Locate every blood parasite and identify its species.
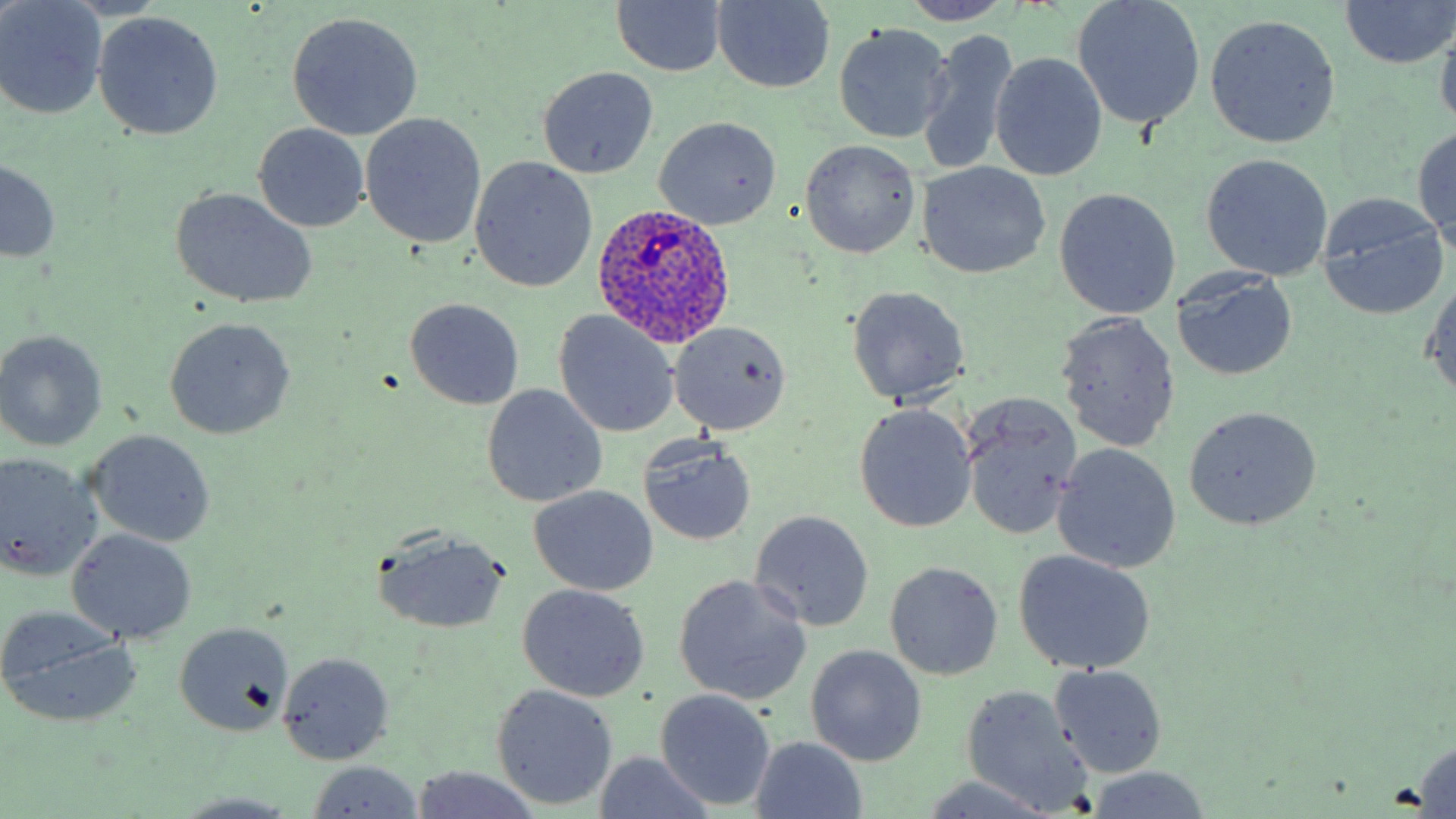

Approximate bounding boxes as (x1,y1)-(x2,y2) corner pairs in pixels.
Plasmodium ovale-infected red blood cells: (591,202)-(737,348).
No Plasmodium falciparum, Plasmodium malariae, Plasmodium vivax, Babesia divergens, or Trypanosoma brucei observed.

Uninfected red blood cell locations: (1340,0)-(1456,71), (0,1)-(107,119), (609,1)-(730,78), (900,1)-(1014,24), (1072,1)-(1206,128), (710,2)-(837,92), (286,11)-(424,140), (92,12)-(225,140), (1205,15)-(1341,147), (1434,20)-(1456,137), (834,22)-(955,144), (919,26)-(1019,177), (990,52)-(1108,182), (538,67)-(660,179), (360,112)-(487,249), (654,117)-(781,230), (1413,122)-(1455,250), (253,123)-(370,232), (800,139)-(921,259), (1200,153)-(1334,281), (469,156)-(598,292), (1,159)-(63,265), (917,161)-(1052,279), (170,188)-(318,309), (1054,188)-(1181,319), (1315,194)-(1449,319), (1172,269)-(1298,383), (1422,275)-(1456,403), (846,286)-(969,405), (405,298)-(524,410), (555,311)-(680,435), (1055,311)-(1183,454), (164,318)-(296,440), (669,321)-(790,435), (0,330)-(110,451), (483,384)-(606,507), (962,388)-(1081,539), (853,405)-(976,531), (1182,407)-(1320,530), (84,430)-(215,547), (639,439)-(756,546), (1051,443)-(1181,574), (0,454)-(100,582), (528,486)-(657,596), (749,510)-(875,632), (66,527)-(197,643), (372,528)-(510,636), (1014,550)-(1156,675), (884,561)-(1003,680), (673,575)-(811,705), (518,584)-(650,701), (0,607)-(139,726), (174,621)-(294,736), (805,644)-(928,767), (276,651)-(395,764), (1050,663)-(1168,777), (957,684)-(1093,814), (491,685)-(619,810), (658,689)-(775,808), (749,736)-(868,818), (1408,740)-(1456,815), (591,753)-(719,819), (307,762)-(424,817), (411,766)-(541,819), (1082,769)-(1213,817), (171,792)-(305,817). Slide-level diagnosis: Plasmodium ovale. Thin blood film. Single field of view. May-Grünwald-Giemsa-stained preparation. 1000x magnification. Light microscopy. Image is 1456×819 pixels.